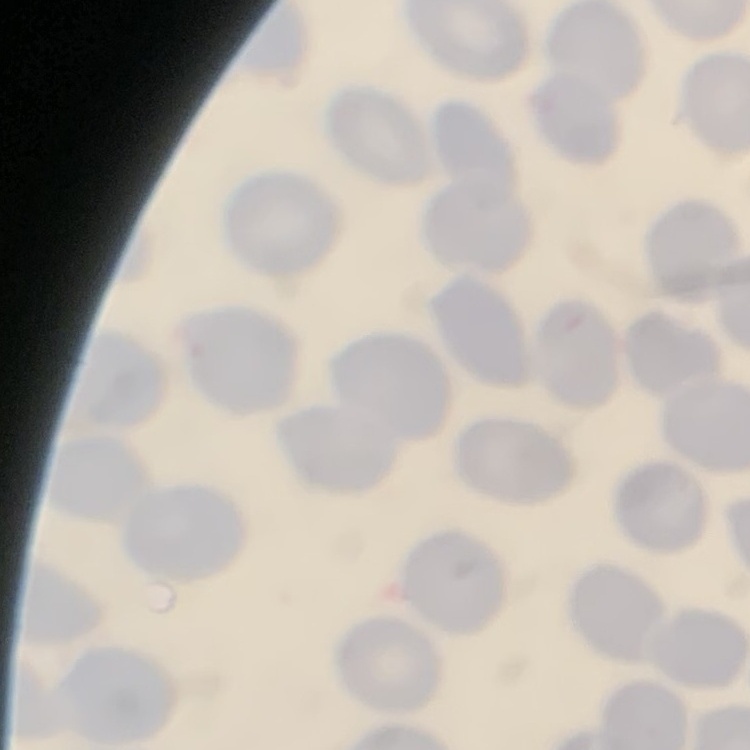
The erythrocytes exhibit no rouleaux formation. Stained with either Field's or Giemsa. Thin peripheral smear. Square crop of a larger photomicrograph.